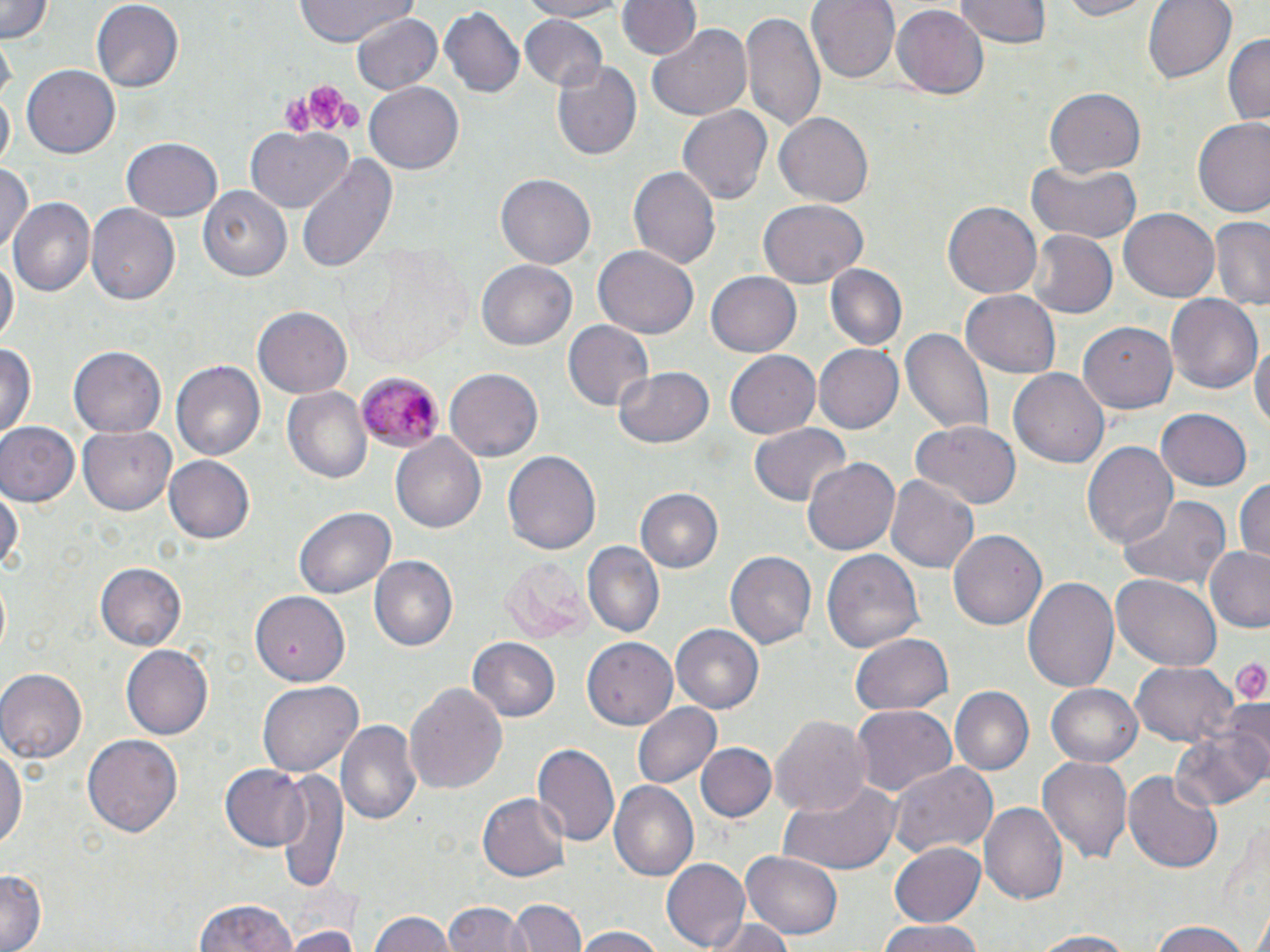

Approximate bounding boxes as (x1, y1, x2, y2) in pixels. Platelet locations: (304, 83, 344, 126), (282, 97, 313, 135), (339, 101, 362, 129), (1229, 654, 1270, 705). Plasmodium malariae-infected red blood cell locations: (358, 371, 443, 452). Uninfected red blood cell locations: (1, 0, 57, 43), (293, 0, 416, 44), (514, 0, 625, 21), (616, 0, 699, 62), (806, 0, 900, 81), (955, 0, 1054, 46), (1045, 0, 1162, 22), (1144, 0, 1236, 83), (89, 1, 183, 92), (888, 4, 990, 101), (438, 5, 524, 98), (743, 9, 827, 137), (351, 12, 440, 97), (517, 14, 608, 93), (646, 24, 753, 120), (1223, 32, 1270, 125), (547, 59, 643, 163), (22, 63, 120, 154), (364, 81, 465, 173), (1, 88, 14, 172), (1044, 89, 1145, 176), (676, 105, 772, 209), (772, 111, 875, 206), (1193, 118, 1270, 220), (245, 127, 353, 213), (122, 136, 222, 221), (293, 156, 398, 277), (1027, 161, 1142, 243), (0, 163, 36, 255), (628, 166, 720, 273), (496, 174, 595, 269), (198, 187, 292, 282), (8, 197, 94, 297), (758, 199, 869, 288), (943, 201, 1041, 299), (86, 203, 180, 304), (1119, 207, 1218, 299), (1211, 217, 1269, 311), (1027, 230, 1117, 318), (349, 244, 472, 369), (592, 244, 699, 340), (0, 255, 17, 345), (477, 260, 578, 350), (824, 265, 906, 352), (706, 269, 802, 356), (961, 288, 1060, 376), (1166, 293, 1262, 397), (253, 307, 353, 397), (562, 320, 655, 411), (900, 324, 993, 436), (1079, 324, 1178, 414), (1250, 337, 1269, 441), (0, 341, 37, 440), (815, 343, 906, 434), (69, 346, 165, 439), (723, 351, 819, 440), (169, 360, 264, 464), (614, 367, 716, 450), (1009, 367, 1110, 468), (445, 369, 543, 461), (281, 387, 371, 485), (1155, 408, 1253, 490), (910, 418, 1022, 511), (0, 422, 78, 507), (79, 423, 179, 514), (748, 423, 852, 505), (390, 434, 487, 534), (1081, 440, 1177, 549), (502, 448, 600, 559), (165, 454, 255, 544), (802, 455, 900, 560), (885, 473, 978, 574), (1232, 477, 1270, 564), (0, 485, 24, 579), (635, 487, 722, 575), (1118, 494, 1233, 590), (293, 506, 395, 602), (949, 528, 1046, 631), (582, 542, 664, 636), (1204, 547, 1270, 631), (725, 549, 817, 648), (823, 549, 925, 653), (368, 556, 458, 652), (501, 556, 587, 642), (96, 564, 185, 649), (1111, 573, 1221, 671), (1023, 576, 1119, 695), (252, 590, 350, 683), (671, 624, 765, 712), (582, 633, 675, 726), (851, 633, 954, 715), (467, 637, 562, 723), (121, 644, 212, 739), (1130, 661, 1237, 746), (0, 668, 88, 762), (259, 678, 362, 774), (406, 681, 507, 796), (1046, 683, 1144, 767), (948, 686, 1034, 776), (631, 701, 721, 789), (852, 705, 957, 798), (771, 712, 870, 818), (336, 719, 422, 829), (1167, 723, 1270, 814), (84, 733, 183, 840), (532, 741, 620, 847), (696, 742, 777, 823), (0, 743, 27, 857), (1036, 749, 1132, 863), (889, 759, 998, 859), (220, 765, 312, 851), (275, 766, 348, 896), (1123, 768, 1222, 875), (987, 777, 1122, 892), (609, 782, 700, 883), (777, 782, 902, 874), (477, 793, 569, 880), (979, 801, 1068, 907), (889, 840, 987, 927), (741, 848, 846, 941), (661, 858, 750, 951), (0, 868, 44, 952), (509, 898, 587, 952), (192, 899, 300, 952), (445, 900, 525, 952), (1250, 908, 1270, 952), (370, 909, 453, 952), (709, 918, 796, 952), (875, 919, 987, 952), (288, 920, 361, 952), (1149, 924, 1252, 952), (575, 926, 664, 952), (1023, 930, 1145, 951). Slide-level diagnosis: Plasmodium malariae. Captured at 1000x magnification. Single field of view. Light microscopy. May-Grünwald-Giemsa-stained preparation. Image is 1270×952 pixels. Thin blood smear.